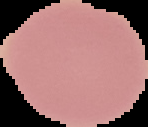
image type = cell region segmented out of the field of view; surrounding area masked to black
image size = 148×127 pixels
preparation = thin blood smear
result = negative for malaria parasites